Outline each blood parasite and name the species.
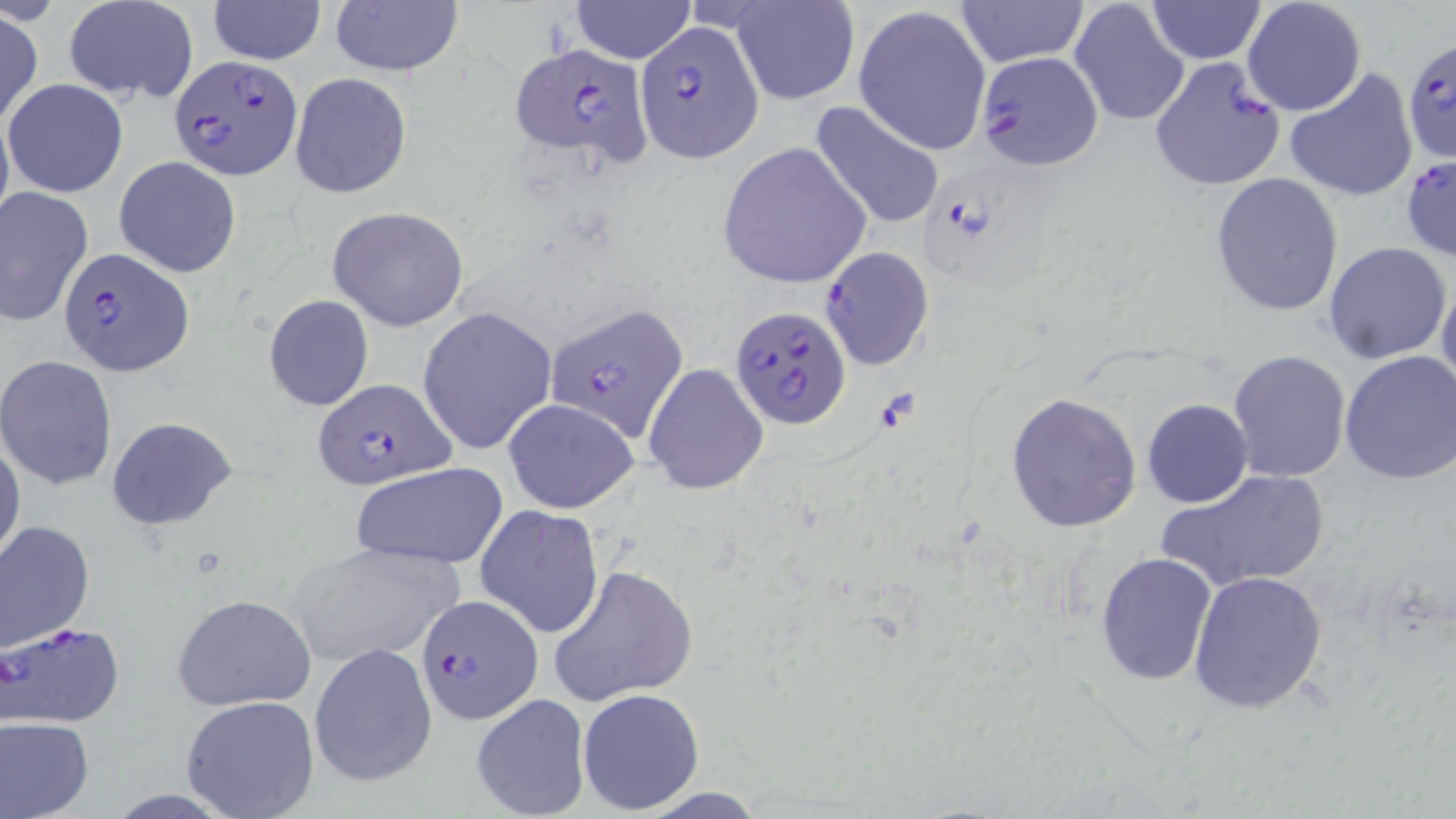

Approximate bounding boxes as (x1,y1)-(x2,y2) corner pairs in pixels.
Plasmodium falciparum-infected red blood cells: (636,22)-(764,160), (507,42)-(652,168), (1406,44)-(1456,165), (975,49)-(1104,170), (169,55)-(302,178), (1149,56)-(1286,191), (1400,154)-(1454,263), (58,244)-(193,375), (818,247)-(935,371), (543,302)-(689,444), (731,304)-(851,429), (308,380)-(460,491), (415,594)-(541,723), (1,620)-(126,727).
No Plasmodium ovale, Plasmodium malariae, Plasmodium vivax, Babesia divergens, or Trypanosoma brucei observed.

slide_level_diagnosis: Plasmodium falciparum
field_of_view: single
magnification: 1000x
preparation: thin blood film
uninfected_red_blood_cell_locations: 'approximate bounding boxes as (x1,y1)-(x2,y2) corner pairs in pixels: (207,0)-(328,66), (731,0)-(859,105), (955,0)-(1090,66), (1145,0)-(1267,63), (1241,0)-(1367,117), (63,1)-(200,104), (329,1)-(464,79), (569,1)-(696,64), (1070,2)-(1191,128), (852,5)-(992,156), (0,10)-(44,125), (1284,68)-(1418,203), (290,72)-(411,198), (3,79)-(129,197), (808,100)-(946,232), (715,144)-(870,288), (114,155)-(242,278), (1210,172)-(1345,316), (0,186)-(94,326), (328,206)-(472,332), (1322,241)-(1453,366), (1436,271)-(1456,400), (263,295)-(375,411), (416,306)-(558,456), (1227,349)-(1350,482), (1336,350)-(1456,486), (0,356)-(118,491), (642,362)-(766,495), (1006,393)-(1142,533), (503,397)-(640,514), (1142,399)-(1252,508), (106,416)-(238,530), (0,436)-(25,569), (351,462)-(507,568), (1163,468)-(1328,593), (475,506)-(606,639), (0,520)-(96,651), (286,538)-(464,667), (1094,552)-(1218,684), (546,564)-(698,705), (1188,570)-(1327,713), (170,593)-(315,711), (308,641)-(438,787), (577,687)-(706,815), (470,693)-(591,818), (180,696)-(320,818), (0,716)-(95,818)'
modality: optical microscopy
stain: May-Grünwald-Giemsa
image_size: 1456×819 pixels